State which parasite is depicted.
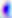
This is Toxoplasma gondii.

Summary:
  - Modality: photomicrograph
  - Magnification: 400x